Assess the morphology of the erythrocytes.
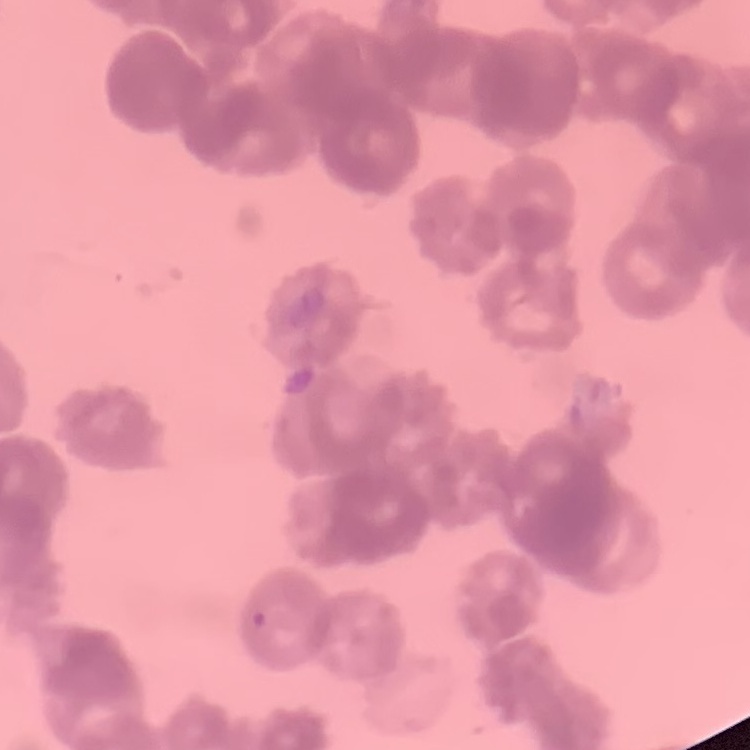

Rouleaux formation.

image type = one tile cut from a larger photomicrograph
preparation = thin peripheral smear
stain = Field's or Giemsa